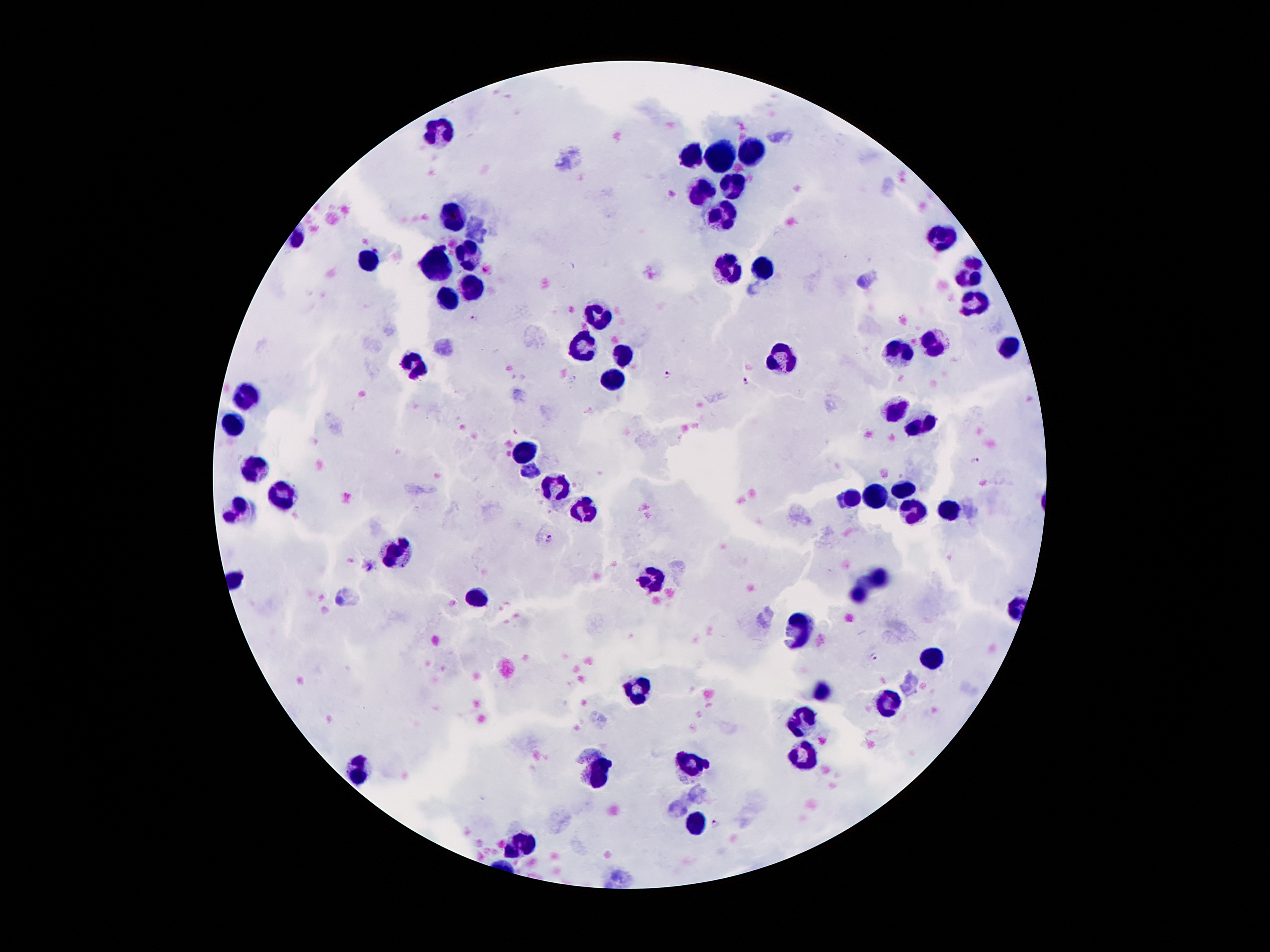

Approximate centers as (x, y) in pixels. Leukocyte locations: (442, 128), (753, 152), (693, 154), (724, 155), (733, 187), (704, 190), (717, 216), (452, 221), (943, 239), (468, 254), (369, 257), (436, 267), (971, 273), (471, 286), (449, 294), (974, 300), (598, 319), (937, 337), (583, 343), (1008, 345), (902, 349), (624, 357), (783, 357), (418, 363), (612, 378), (248, 393), (899, 413), (232, 422), (919, 427), (530, 451), (256, 465), (554, 485), (903, 489), (875, 494), (284, 496), (854, 497), (239, 507), (949, 509), (585, 510), (918, 514), (396, 551), (878, 578), (651, 579), (859, 593), (480, 594), (801, 626), (931, 658), (641, 688), (822, 690), (888, 701), (801, 721), (804, 754), (694, 764), (356, 769), (602, 774), (697, 821), (523, 845). Malaria parasite locations: (473, 319), (668, 372), (747, 381), (976, 461), (550, 538), (370, 567), (874, 655), (716, 824). Patient malaria status: positive for Plasmodium falciparum. 100x magnification. Giemsa stain. Single field of view. Photographed through the microscope eyepiece with a smartphone camera. Thick peripheral-blood smear. Image is 1270×952 pixels.